Identify the cell.
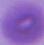

An erythrocyte.

modality: photomicrograph
magnification: 1000x